Describe the morphology of the red blood cells.
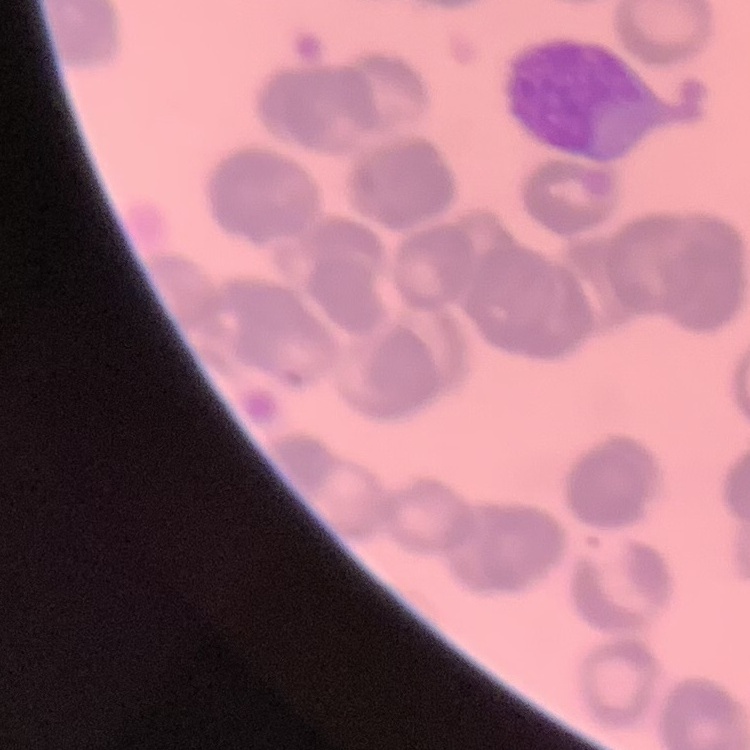

They show rouleaux formation.

Field's or Giemsa stain. One tile cut from a larger photomicrograph. Thin peripheral smear.